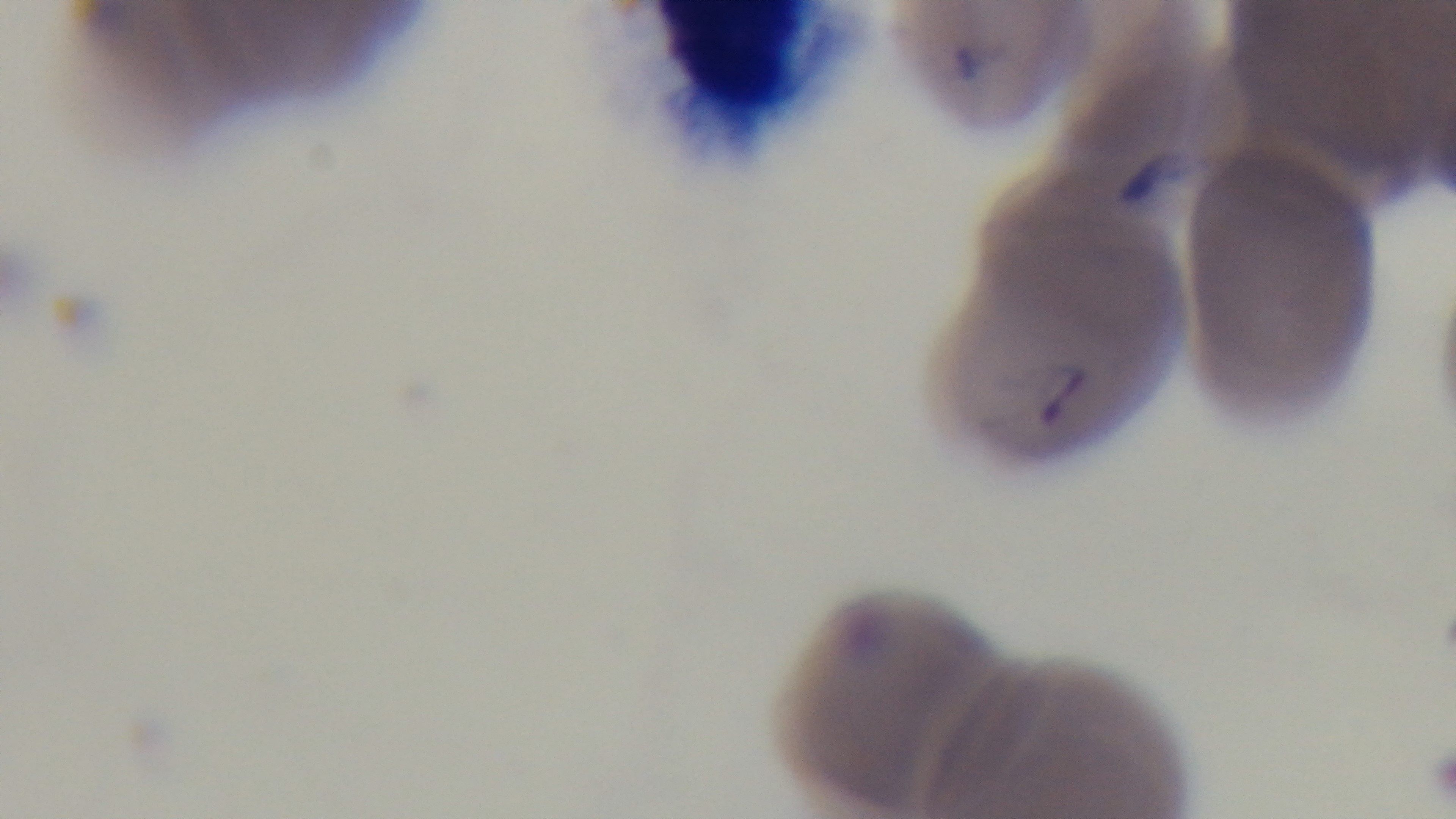
Oil-immersion objective, 100x. Giemsa stain. Mounted 4K digital camera. One field from the slide. Photomicrograph. Malaria status: positive. Preparation: thin blood film.